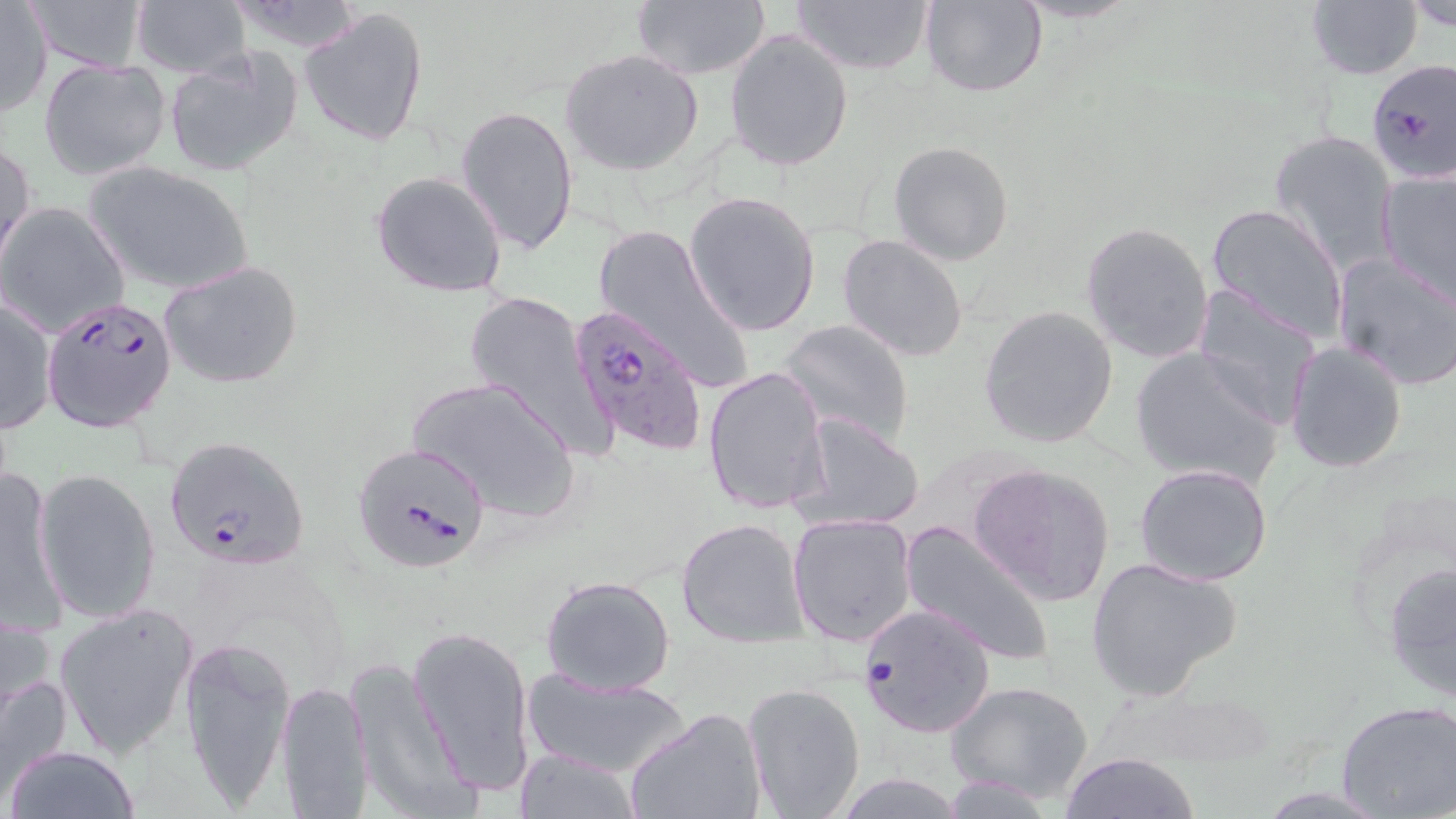
{
  "slide_level_diagnosis": "Plasmodium falciparum",
  "stain": "May-Grünwald-Giemsa",
  "plasmodium_falciparum_infected_red_blood_cell_locations": "approximate bounding boxes as (x1, y1, x2, y2) in pixels: (1367, 60, 1456, 188), (42, 294, 179, 434), (569, 305, 709, 456), (164, 436, 311, 572), (352, 440, 492, 574), (857, 602, 997, 739)",
  "uninfected_red_blood_cell_locations": "approximate bounding boxes as (x1, y1, x2, y2) in pixels: (22, 0, 153, 72), (223, 0, 370, 54), (790, 0, 934, 76), (920, 0, 1048, 98), (1010, 0, 1145, 24), (1305, 0, 1425, 80), (1399, 0, 1456, 31), (631, 1, 771, 80), (131, 2, 251, 77), (1, 3, 52, 117), (298, 6, 429, 147), (724, 29, 854, 171), (559, 48, 704, 175), (162, 49, 304, 178), (38, 59, 170, 180), (457, 103, 579, 255), (1269, 129, 1398, 274), (1, 139, 35, 272), (889, 140, 1014, 266), (81, 161, 254, 294), (1377, 170, 1456, 304), (371, 171, 510, 298), (683, 190, 822, 336), (1204, 202, 1350, 344), (0, 203, 131, 338), (594, 221, 752, 394), (1081, 221, 1215, 363), (836, 232, 969, 361), (1331, 254, 1456, 390), (160, 261, 304, 390), (1192, 289, 1323, 432), (463, 290, 604, 450), (1, 295, 56, 435), (978, 307, 1118, 449), (780, 319, 915, 447), (1283, 339, 1407, 473), (1129, 348, 1285, 488), (703, 365, 830, 515), (407, 375, 582, 523), (796, 413, 924, 532), (969, 462, 1116, 607), (1134, 463, 1275, 586), (1, 467, 66, 632), (35, 469, 162, 625), (787, 513, 917, 647), (677, 516, 809, 647), (900, 521, 1054, 667), (1085, 557, 1240, 702), (1382, 560, 1456, 707), (540, 575, 675, 695), (54, 603, 198, 760), (1, 606, 61, 747), (407, 623, 536, 800), (180, 636, 296, 812), (346, 654, 470, 814), (521, 668, 694, 779), (276, 678, 372, 817), (741, 680, 867, 817), (946, 680, 1095, 805), (1336, 699, 1456, 819), (627, 707, 767, 819), (6, 746, 140, 819), (514, 748, 642, 819), (1062, 752, 1198, 819), (835, 775, 966, 816)",
  "preparation": "thin blood film",
  "magnification": "1000x",
  "field_of_view": "one of a larger specimen",
  "image_size": "1456×819 pixels",
  "modality": "optical microscopy"
}